Mark where cells are.
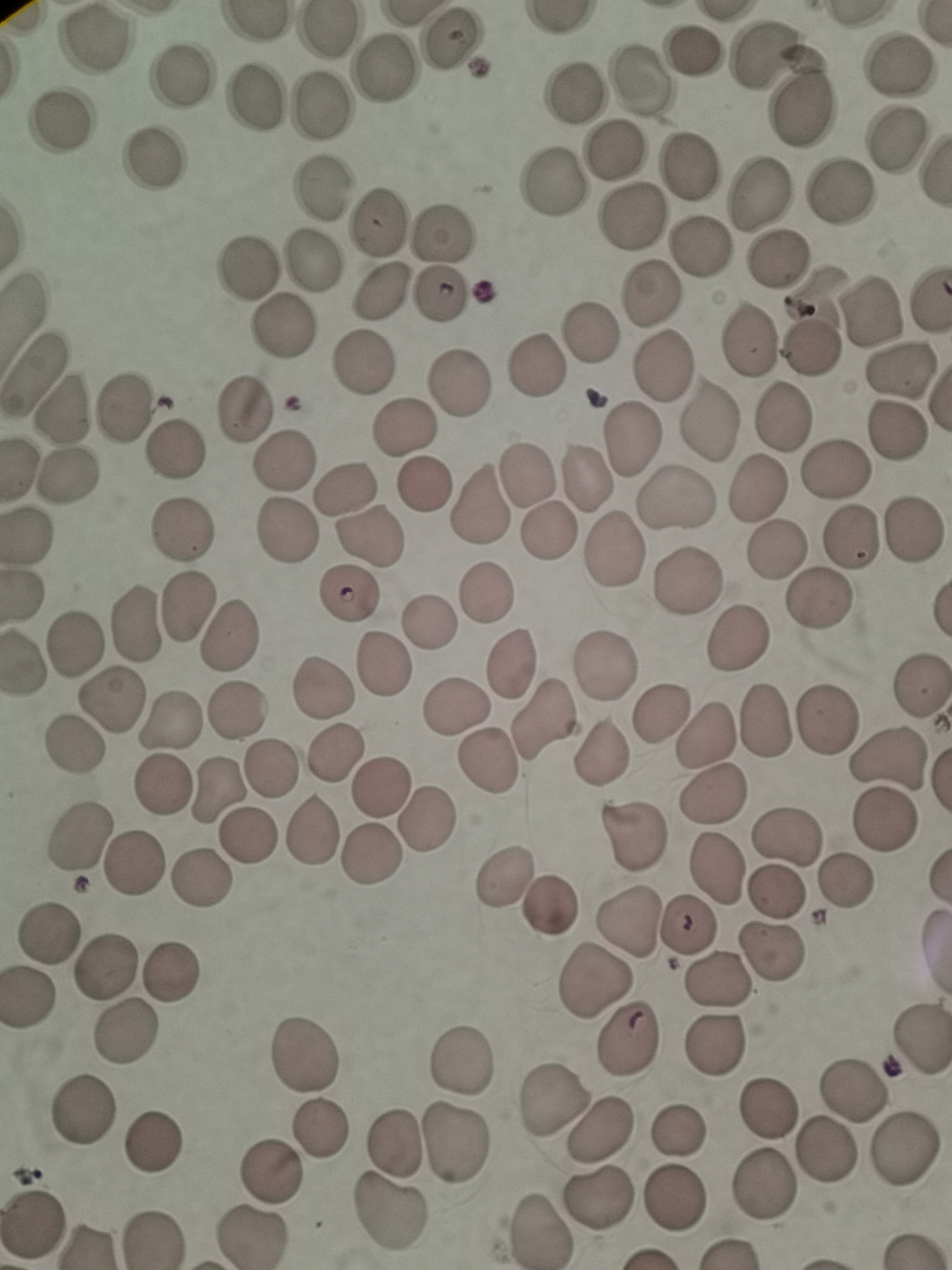
Approximate centers as [x, y] in pixels.
Cells: [95, 39], [451, 41], [694, 50], [762, 57], [900, 66], [382, 68], [181, 75], [643, 80], [573, 97], [253, 99], [319, 105], [802, 108], [62, 125], [897, 141], [615, 153], [160, 157], [691, 167], [322, 187], [840, 194], [759, 196], [634, 215], [375, 222], [444, 236], [700, 247], [779, 257], [311, 260], [248, 266], [383, 292], [650, 292], [819, 293], [438, 296], [874, 313], [592, 328], [281, 331], [750, 341], [815, 351], [364, 361], [663, 362], [535, 367], [34, 369], [898, 370], [461, 386], [127, 406], [242, 407], [68, 408], [781, 417], [710, 419], [405, 428], [899, 431], [632, 439], [171, 455], [282, 459], [837, 472], [69, 473], [529, 473], [589, 474], [427, 484], [348, 486], [755, 487], [679, 500], [481, 504], [284, 529], [550, 530], [914, 530], [181, 531], [24, 536], [371, 537], [850, 537], [776, 549], [615, 550], [687, 585], [350, 593], [487, 594], [21, 597], [820, 599], [188, 605], [134, 621], [430, 624], [231, 632], [76, 638], [739, 640], [382, 662], [26, 663], [511, 665], [605, 667], [320, 684], [920, 686], [113, 698], [458, 708], [238, 709], [660, 710], [170, 718], [826, 721], [543, 723], [766, 723], [705, 731], [74, 742], [601, 753], [334, 756], [888, 759], [487, 760], [271, 768], [162, 784], [383, 785], [215, 793], [712, 793], [426, 821], [887, 822], [312, 832], [83, 833], [630, 834], [784, 834], [250, 836], [373, 855], [135, 866], [717, 866], [504, 876], [202, 881], [847, 886], [778, 891], [552, 907], [627, 921], [688, 927], [49, 931], [774, 951], [105, 965], [177, 971], [721, 982], [597, 983], [25, 998], [126, 1033], [917, 1039], [716, 1041], [627, 1044], [304, 1050], [463, 1058], [857, 1088], [552, 1097], [82, 1110], [767, 1110], [679, 1126], [319, 1127], [600, 1129], [156, 1141], [392, 1145], [459, 1147], [825, 1151], [903, 1153], [269, 1171], [762, 1189], [597, 1196], [672, 1200], [391, 1212], [32, 1222], [534, 1231], [154, 1237], [253, 1237].

One field from this slide. Thin smear of blood. Acquired by smartphone through the microscope eyepiece. Image is 952×1270 pixels. Giemsa-stained preparation.